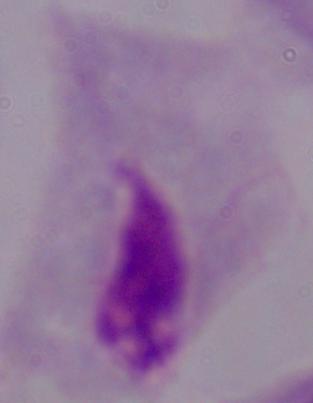
Micrograph. 1000x magnification. A trichomonad is shown.